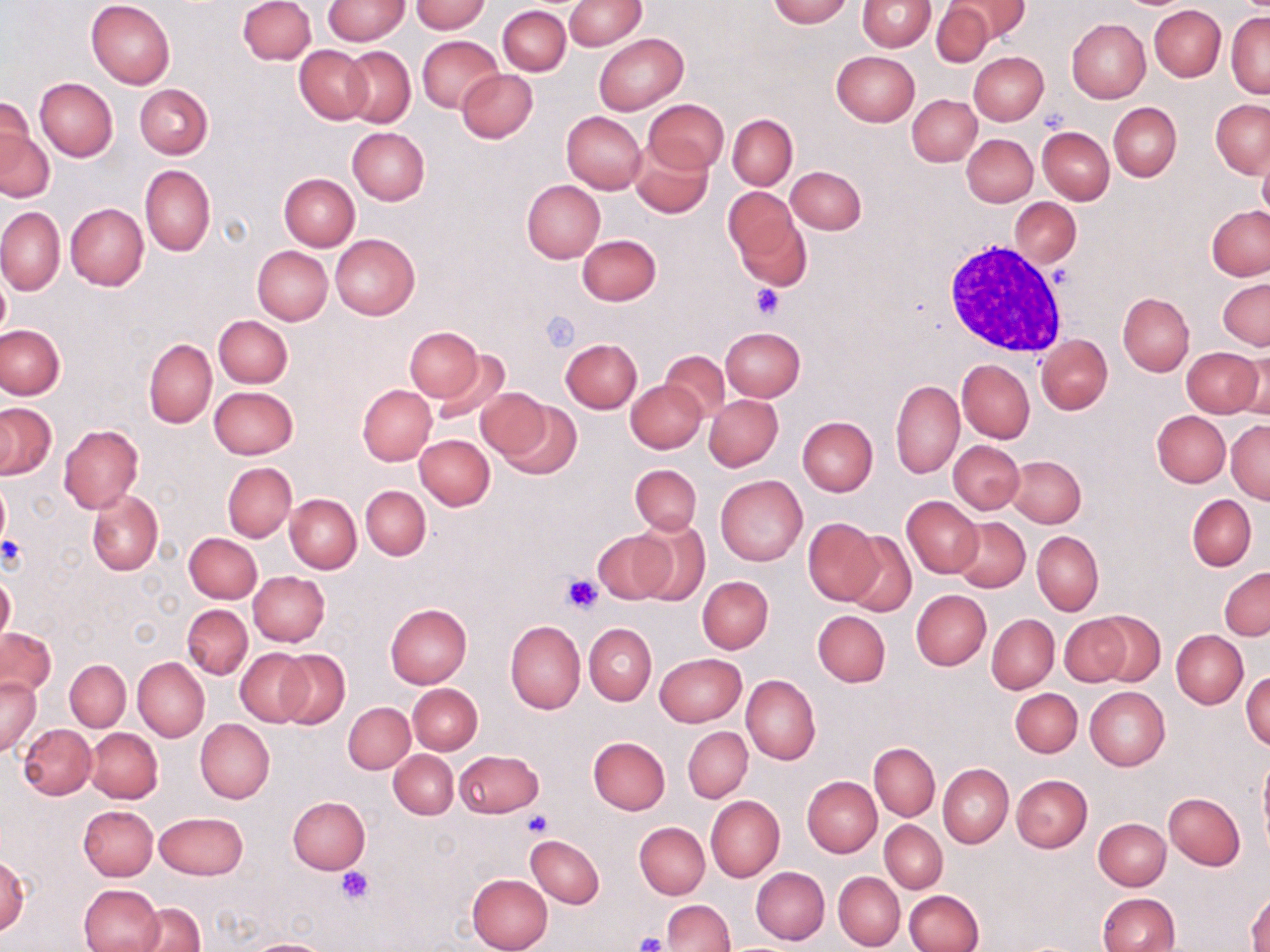

slide-level diagnosis = no evidence of blood parasites
modality = optical microscopy
preparation = thin blood film
uninfected red blood cell locations = approximate bounding boxes as named x1/y1/x2/y2 corners in pixels: (x1=86, y1=0, x2=175, y2=88), (x1=238, y1=0, x2=315, y2=64), (x1=564, y1=0, x2=646, y2=50), (x1=767, y1=0, x2=852, y2=27), (x1=858, y1=0, x2=935, y2=51), (x1=951, y1=0, x2=1028, y2=44), (x1=323, y1=1, x2=410, y2=44), (x1=410, y1=1, x2=490, y2=33), (x1=932, y1=2, x2=993, y2=67), (x1=498, y1=5, x2=571, y2=75), (x1=1149, y1=5, x2=1225, y2=82), (x1=1227, y1=12, x2=1269, y2=99), (x1=1067, y1=19, x2=1149, y2=102), (x1=594, y1=33, x2=687, y2=115), (x1=417, y1=35, x2=504, y2=114), (x1=295, y1=46, x2=372, y2=124), (x1=342, y1=47, x2=416, y2=127), (x1=832, y1=51, x2=920, y2=126), (x1=969, y1=51, x2=1049, y2=125), (x1=457, y1=69, x2=537, y2=143), (x1=34, y1=79, x2=117, y2=162), (x1=135, y1=84, x2=213, y2=158), (x1=907, y1=94, x2=981, y2=166), (x1=644, y1=99, x2=728, y2=174), (x1=1211, y1=100, x2=1270, y2=178), (x1=0, y1=102, x2=49, y2=201), (x1=1109, y1=102, x2=1181, y2=181), (x1=562, y1=112, x2=647, y2=193), (x1=727, y1=114, x2=798, y2=189), (x1=347, y1=126, x2=430, y2=204), (x1=1037, y1=126, x2=1114, y2=204), (x1=962, y1=134, x2=1037, y2=207), (x1=630, y1=143, x2=714, y2=218), (x1=1257, y1=150, x2=1270, y2=225), (x1=140, y1=165, x2=216, y2=257), (x1=787, y1=166, x2=866, y2=234), (x1=279, y1=174, x2=360, y2=250), (x1=521, y1=179, x2=605, y2=263), (x1=722, y1=187, x2=806, y2=285), (x1=1009, y1=198, x2=1080, y2=268), (x1=65, y1=204, x2=148, y2=291), (x1=1207, y1=206, x2=1270, y2=279), (x1=0, y1=207, x2=65, y2=294), (x1=330, y1=233, x2=421, y2=320), (x1=577, y1=234, x2=661, y2=306), (x1=252, y1=246, x2=332, y2=324), (x1=0, y1=271, x2=10, y2=339), (x1=1219, y1=277, x2=1270, y2=350), (x1=1118, y1=292, x2=1194, y2=375), (x1=213, y1=315, x2=292, y2=388), (x1=0, y1=325, x2=65, y2=399), (x1=721, y1=327, x2=805, y2=401), (x1=405, y1=328, x2=480, y2=399), (x1=1037, y1=334, x2=1112, y2=414), (x1=560, y1=339, x2=642, y2=413), (x1=144, y1=340, x2=216, y2=427), (x1=1182, y1=346, x2=1263, y2=416), (x1=429, y1=350, x2=509, y2=425), (x1=661, y1=350, x2=730, y2=420), (x1=1240, y1=350, x2=1270, y2=421), (x1=957, y1=359, x2=1034, y2=443), (x1=626, y1=379, x2=707, y2=454), (x1=891, y1=380, x2=964, y2=478), (x1=358, y1=384, x2=437, y2=465), (x1=210, y1=386, x2=298, y2=459), (x1=477, y1=388, x2=551, y2=461), (x1=703, y1=395, x2=782, y2=471), (x1=501, y1=401, x2=581, y2=479), (x1=0, y1=403, x2=56, y2=479), (x1=1153, y1=411, x2=1230, y2=487), (x1=797, y1=416, x2=877, y2=496), (x1=1227, y1=421, x2=1270, y2=502), (x1=58, y1=424, x2=143, y2=514), (x1=415, y1=434, x2=494, y2=509), (x1=950, y1=441, x2=1024, y2=514), (x1=1006, y1=455, x2=1086, y2=528), (x1=222, y1=463, x2=296, y2=541), (x1=630, y1=464, x2=702, y2=535), (x1=716, y1=475, x2=807, y2=565), (x1=0, y1=479, x2=10, y2=550), (x1=361, y1=485, x2=430, y2=560), (x1=86, y1=490, x2=162, y2=576), (x1=284, y1=494, x2=361, y2=573), (x1=1188, y1=494, x2=1256, y2=570), (x1=902, y1=497, x2=983, y2=577), (x1=952, y1=516, x2=1030, y2=593), (x1=802, y1=518, x2=884, y2=606), (x1=630, y1=519, x2=710, y2=606), (x1=593, y1=529, x2=675, y2=605), (x1=1032, y1=531, x2=1104, y2=616), (x1=184, y1=532, x2=262, y2=603), (x1=845, y1=532, x2=916, y2=615), (x1=1219, y1=566, x2=1270, y2=639), (x1=1, y1=570, x2=15, y2=646), (x1=249, y1=571, x2=330, y2=646), (x1=697, y1=575, x2=773, y2=653), (x1=910, y1=590, x2=991, y2=670), (x1=183, y1=604, x2=252, y2=678), (x1=385, y1=604, x2=473, y2=688), (x1=813, y1=610, x2=890, y2=687), (x1=1089, y1=612, x2=1165, y2=686), (x1=987, y1=614, x2=1058, y2=693), (x1=1060, y1=614, x2=1133, y2=686), (x1=505, y1=620, x2=586, y2=713), (x1=584, y1=624, x2=656, y2=705), (x1=1, y1=627, x2=57, y2=697), (x1=1172, y1=630, x2=1248, y2=708), (x1=235, y1=649, x2=312, y2=727), (x1=276, y1=650, x2=350, y2=728), (x1=655, y1=653, x2=746, y2=727), (x1=133, y1=657, x2=209, y2=742), (x1=65, y1=659, x2=130, y2=730), (x1=1241, y1=668, x2=1270, y2=750), (x1=741, y1=674, x2=820, y2=765), (x1=0, y1=677, x2=41, y2=757), (x1=408, y1=683, x2=483, y2=754), (x1=1085, y1=686, x2=1170, y2=770), (x1=1010, y1=688, x2=1082, y2=757), (x1=343, y1=702, x2=414, y2=773), (x1=195, y1=719, x2=274, y2=803), (x1=19, y1=723, x2=96, y2=799), (x1=683, y1=727, x2=752, y2=802), (x1=86, y1=728, x2=162, y2=802), (x1=588, y1=736, x2=670, y2=814), (x1=871, y1=743, x2=939, y2=820), (x1=454, y1=749, x2=543, y2=817), (x1=389, y1=750, x2=458, y2=818), (x1=1259, y1=753, x2=1270, y2=851), (x1=939, y1=764, x2=1013, y2=848), (x1=1012, y1=774, x2=1092, y2=852), (x1=802, y1=776, x2=881, y2=857), (x1=1164, y1=792, x2=1245, y2=870), (x1=706, y1=796, x2=784, y2=881), (x1=288, y1=797, x2=370, y2=874), (x1=78, y1=805, x2=158, y2=880), (x1=154, y1=811, x2=248, y2=879), (x1=1095, y1=811, x2=1237, y2=882), (x1=1093, y1=818, x2=1170, y2=889), (x1=880, y1=820, x2=948, y2=893), (x1=635, y1=822, x2=709, y2=899), (x1=526, y1=834, x2=604, y2=908), (x1=0, y1=857, x2=28, y2=935), (x1=751, y1=867, x2=829, y2=945), (x1=834, y1=872, x2=904, y2=950), (x1=467, y1=874, x2=553, y2=952), (x1=78, y1=884, x2=164, y2=952), (x1=1248, y1=887, x2=1269, y2=952), (x1=904, y1=890, x2=984, y2=952), (x1=1097, y1=893, x2=1178, y2=952), (x1=661, y1=899, x2=734, y2=951), (x1=135, y1=903, x2=206, y2=952), (x1=245, y1=938, x2=335, y2=952)
field of view = single
stain = May-Grünwald-Giemsa
white blood cell locations = approximate bounding boxes as named x1/y1/x2/y2 corners in pixels: (x1=940, y1=237, x2=1067, y2=361)
magnification = 1000x
platelet locations = approximate bounding boxes as named x1/y1/x2/y2 corners in pixels: (x1=751, y1=282, x2=782, y2=318), (x1=541, y1=311, x2=580, y2=351), (x1=0, y1=536, x2=25, y2=568), (x1=561, y1=573, x2=604, y2=613), (x1=523, y1=810, x2=552, y2=836), (x1=336, y1=867, x2=372, y2=904), (x1=635, y1=932, x2=667, y2=952)
image size = 1270×952 pixels